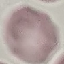
result = no malaria parasites detected
stain = Giemsa
preparation = thin blood smear
capture = smartphone camera at the microscope eyepiece
image type = automatically extracted cell patch, resized to 64 × 64 pixels